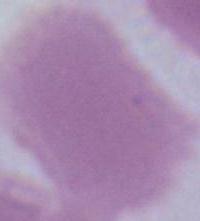
A red blood cell is seen. Micrograph. Captured at 1000x magnification.